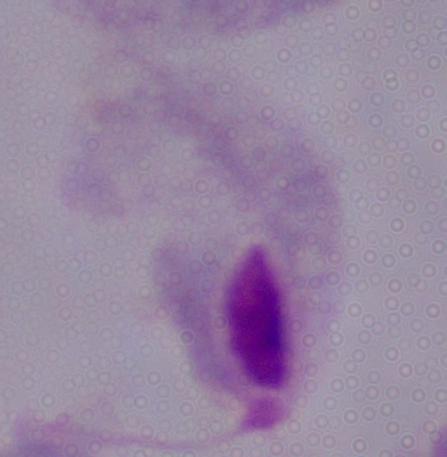
identification = trichomonad
modality = micrograph
magnification = 1000x